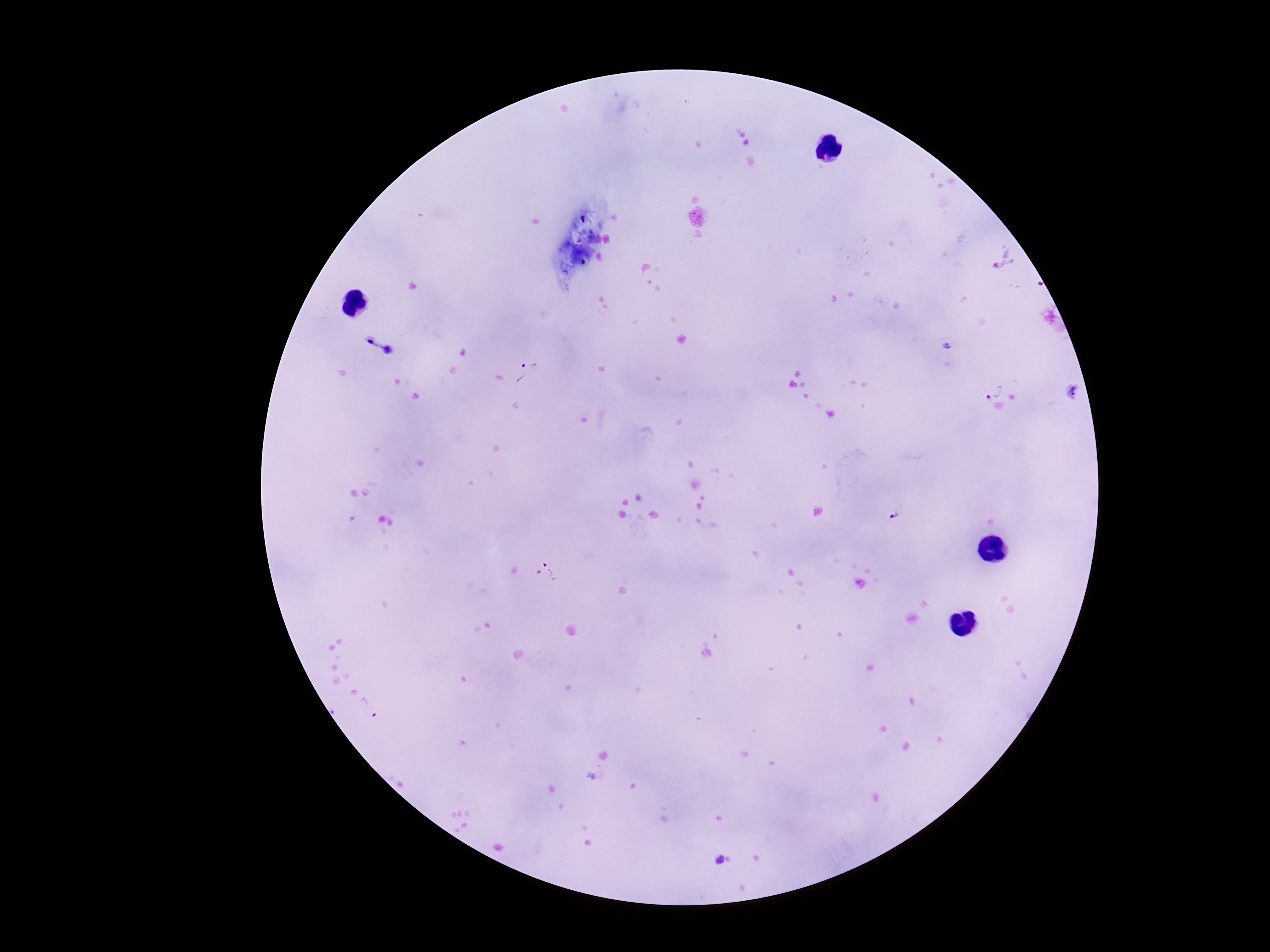
Approximate centers as (x, y) in pixels.
Summary:
  - Plasmodium parasite locations: (1003, 261), (376, 348), (529, 374), (993, 388), (896, 514), (545, 570), (373, 706), (723, 858)
  - Magnification: 100x
  - Image size: 1270×952 pixels
  - Preparation: thick peripheral-blood smear
  - Capture: smartphone camera through the microscope eyepiece
  - Field of view: one from this slide
  - Stain: Giemsa
  - Patient malaria status: positive